Outline each uninfected red blood cell.
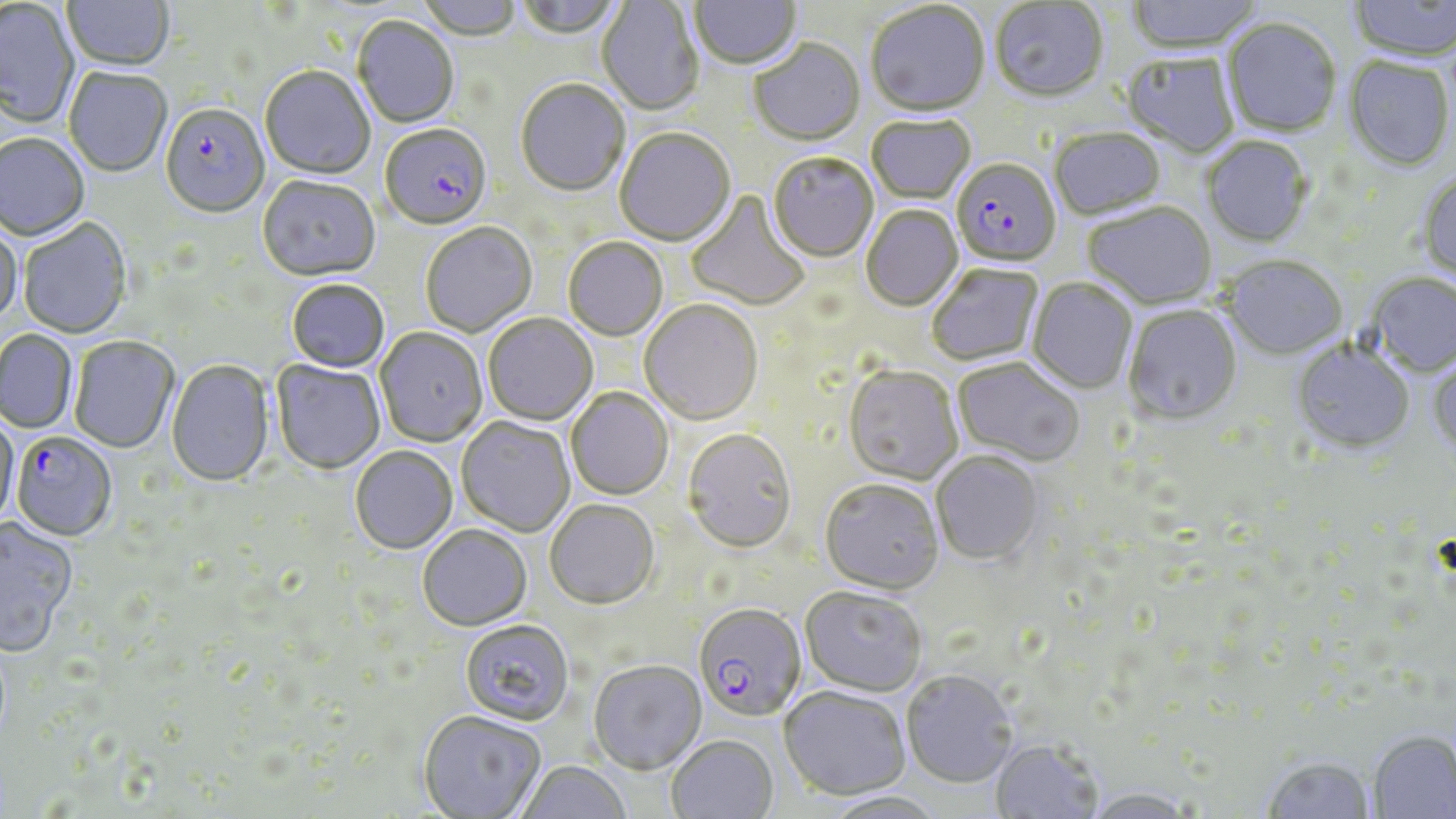
Approximate bounding boxes as named x1/y1/x2/y2 corners in pixels.
Uninfected red blood cells: (x1=62, y1=0, x2=175, y2=74), (x1=415, y1=0, x2=521, y2=43), (x1=513, y1=0, x2=624, y2=42), (x1=689, y1=0, x2=801, y2=72), (x1=1126, y1=0, x2=1264, y2=56), (x1=1348, y1=0, x2=1456, y2=64), (x1=597, y1=1, x2=704, y2=116), (x1=990, y1=1, x2=1109, y2=105), (x1=0, y1=2, x2=80, y2=130), (x1=866, y1=3, x2=990, y2=120), (x1=352, y1=17, x2=459, y2=129), (x1=1221, y1=20, x2=1341, y2=139), (x1=749, y1=41, x2=865, y2=148), (x1=1121, y1=54, x2=1240, y2=159), (x1=1343, y1=57, x2=1454, y2=173), (x1=260, y1=67, x2=375, y2=181), (x1=63, y1=68, x2=172, y2=179), (x1=515, y1=81, x2=630, y2=199), (x1=866, y1=117, x2=975, y2=206), (x1=615, y1=129, x2=736, y2=247), (x1=1050, y1=129, x2=1166, y2=222), (x1=0, y1=135, x2=90, y2=244), (x1=1202, y1=137, x2=1313, y2=248), (x1=768, y1=154, x2=878, y2=264), (x1=1418, y1=169, x2=1456, y2=285), (x1=258, y1=177, x2=381, y2=283), (x1=685, y1=190, x2=811, y2=312), (x1=1083, y1=203, x2=1217, y2=310), (x1=862, y1=206, x2=963, y2=312), (x1=18, y1=219, x2=133, y2=340), (x1=0, y1=223, x2=23, y2=327), (x1=420, y1=223, x2=537, y2=337), (x1=563, y1=238, x2=668, y2=342), (x1=1219, y1=257, x2=1348, y2=362), (x1=926, y1=263, x2=1043, y2=367), (x1=1367, y1=274, x2=1456, y2=378), (x1=1027, y1=278, x2=1137, y2=395), (x1=286, y1=280, x2=390, y2=374), (x1=639, y1=300, x2=763, y2=426), (x1=1123, y1=306, x2=1242, y2=427), (x1=483, y1=314, x2=598, y2=426), (x1=375, y1=328, x2=488, y2=447), (x1=0, y1=331, x2=78, y2=435), (x1=69, y1=337, x2=179, y2=455), (x1=1291, y1=342, x2=1415, y2=455), (x1=1427, y1=354, x2=1456, y2=460), (x1=951, y1=358, x2=1084, y2=467), (x1=271, y1=359, x2=385, y2=474), (x1=166, y1=360, x2=274, y2=488), (x1=843, y1=366, x2=963, y2=485), (x1=566, y1=387, x2=674, y2=500), (x1=0, y1=413, x2=20, y2=531), (x1=456, y1=416, x2=576, y2=537), (x1=681, y1=428, x2=797, y2=553), (x1=350, y1=446, x2=457, y2=554), (x1=931, y1=452, x2=1044, y2=564), (x1=819, y1=479, x2=945, y2=595), (x1=545, y1=498, x2=659, y2=609), (x1=1, y1=517, x2=79, y2=656), (x1=417, y1=524, x2=532, y2=630), (x1=800, y1=586, x2=927, y2=697), (x1=459, y1=619, x2=574, y2=725), (x1=589, y1=659, x2=706, y2=774), (x1=901, y1=670, x2=1018, y2=788), (x1=779, y1=687, x2=911, y2=801), (x1=417, y1=710, x2=547, y2=818), (x1=1368, y1=732, x2=1456, y2=818), (x1=666, y1=734, x2=779, y2=819), (x1=990, y1=740, x2=1103, y2=819), (x1=1261, y1=756, x2=1376, y2=818), (x1=514, y1=760, x2=632, y2=819), (x1=1083, y1=787, x2=1198, y2=819), (x1=819, y1=791, x2=948, y2=819).

{
  "slide_level_diagnosis": "Plasmodium falciparum",
  "field_of_view": "one of a larger specimen",
  "image_size": "1456×819 pixels",
  "modality": "light microscopy",
  "preparation": "thin blood film",
  "stain": "May-Grünwald-Giemsa",
  "magnification": "1000x",
  "plasmodium_falciparum_infected_red_blood_cell_locations": "approximate bounding boxes as named x1/y1/x2/y2 corners in pixels: (x1=160, y1=105, x2=270, y2=220), (x1=381, y1=125, x2=492, y2=231), (x1=952, y1=160, x2=1061, y2=269), (x1=10, y1=433, x2=117, y2=543), (x1=693, y1=603, x2=808, y2=721)"
}